Report the malaria status of this cell.
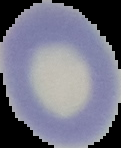
It is uninfected.

Summary:
  - Image type: segmented cell region on a black background
  - Preparation: thin blood film
  - Image size: 121×148 pixels